Comment on the morphology of the erythrocytes.
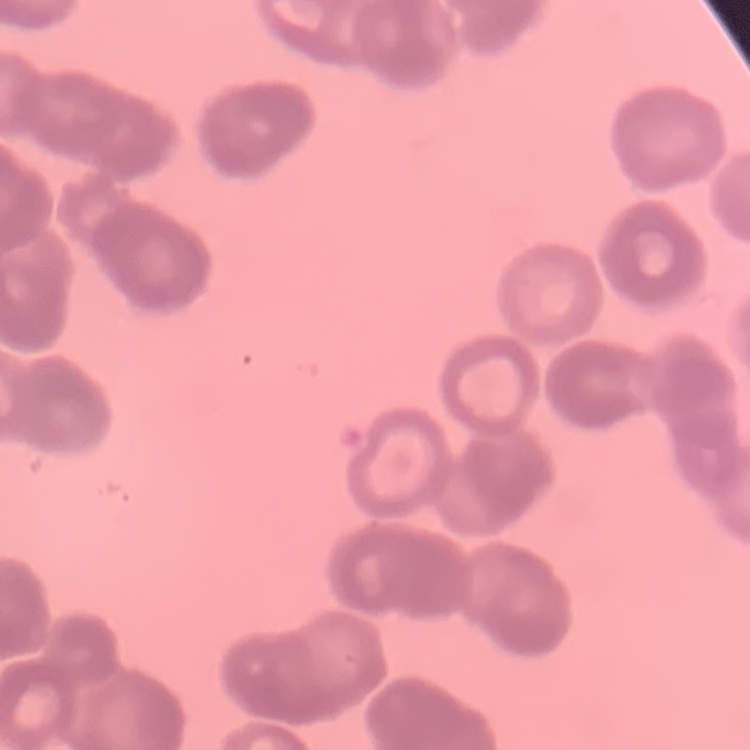
Rouleaux formation.

preparation: thin blood smear
image_type: one tile cut from a larger photomicrograph
stain: Field's or Giemsa